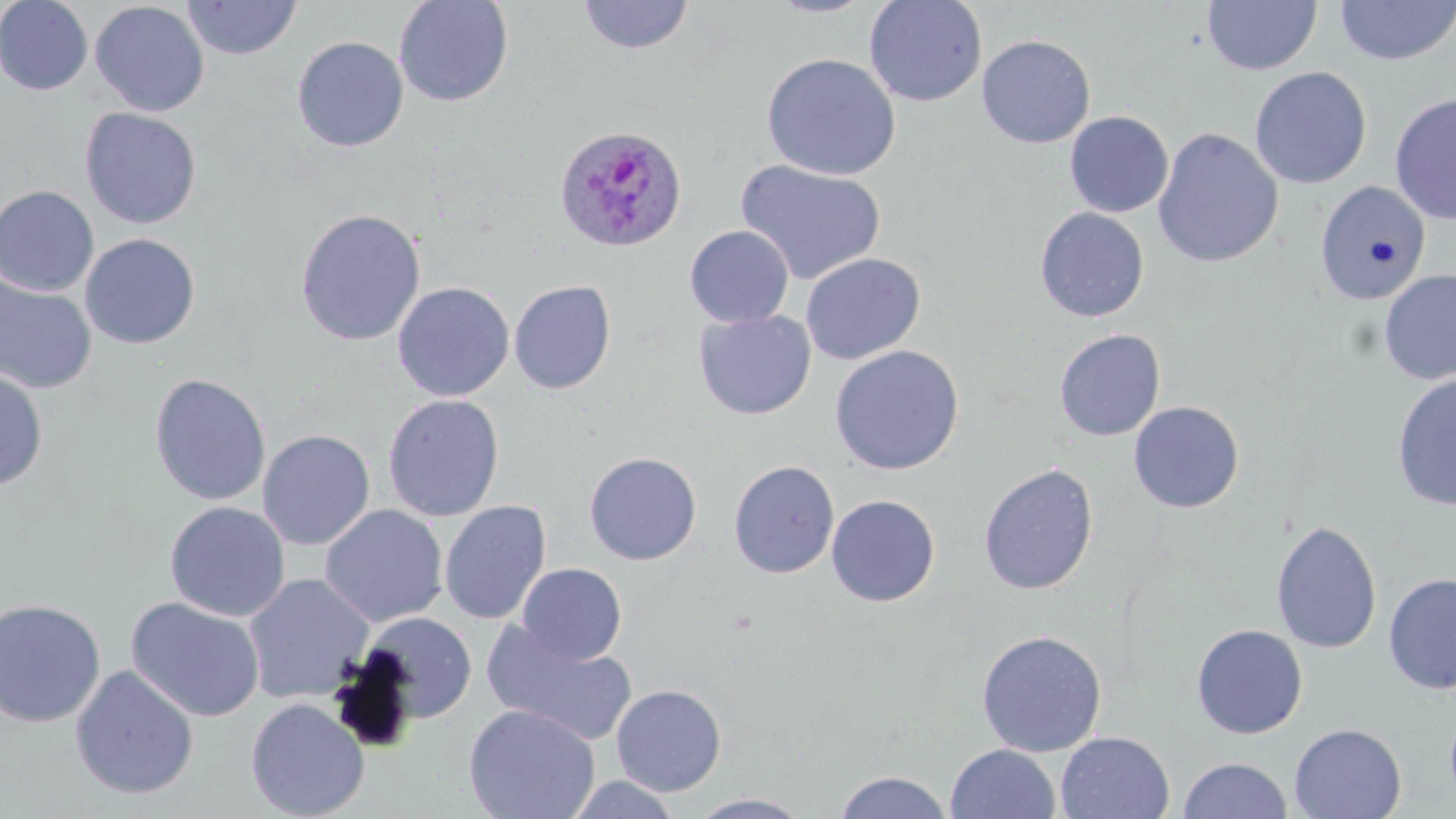 Approximate bounding boxes as named x1/y1/x2/y2 corners in pixels. Uninfected red blood cell locations: (x1=0, y1=0, x2=94, y2=95), (x1=182, y1=0, x2=302, y2=60), (x1=393, y1=0, x2=513, y2=107), (x1=577, y1=0, x2=695, y2=55), (x1=764, y1=0, x2=879, y2=18), (x1=864, y1=0, x2=987, y2=107), (x1=1202, y1=0, x2=1321, y2=75), (x1=1334, y1=0, x2=1456, y2=66), (x1=89, y1=1, x2=210, y2=117), (x1=976, y1=34, x2=1096, y2=148), (x1=292, y1=36, x2=409, y2=152), (x1=762, y1=53, x2=901, y2=180), (x1=1250, y1=66, x2=1372, y2=189), (x1=1389, y1=92, x2=1456, y2=225), (x1=79, y1=107, x2=202, y2=229), (x1=1065, y1=111, x2=1174, y2=217), (x1=1152, y1=127, x2=1284, y2=268), (x1=735, y1=159, x2=887, y2=285), (x1=1313, y1=181, x2=1431, y2=305), (x1=0, y1=185, x2=100, y2=297), (x1=1035, y1=207, x2=1150, y2=322), (x1=294, y1=209, x2=426, y2=346), (x1=685, y1=225, x2=794, y2=328), (x1=79, y1=233, x2=200, y2=349), (x1=799, y1=253, x2=926, y2=364), (x1=1378, y1=269, x2=1456, y2=385), (x1=0, y1=274, x2=97, y2=394), (x1=509, y1=279, x2=616, y2=395), (x1=392, y1=281, x2=515, y2=402), (x1=694, y1=310, x2=816, y2=420), (x1=1053, y1=329, x2=1165, y2=441), (x1=829, y1=345, x2=964, y2=476), (x1=0, y1=367, x2=49, y2=491), (x1=150, y1=373, x2=271, y2=506), (x1=1391, y1=374, x2=1456, y2=512), (x1=382, y1=394, x2=505, y2=522), (x1=1129, y1=401, x2=1244, y2=513), (x1=257, y1=429, x2=375, y2=550), (x1=584, y1=451, x2=702, y2=565), (x1=728, y1=460, x2=839, y2=579), (x1=978, y1=462, x2=1098, y2=595), (x1=826, y1=494, x2=940, y2=607), (x1=439, y1=500, x2=551, y2=625), (x1=164, y1=501, x2=290, y2=622), (x1=319, y1=504, x2=448, y2=627), (x1=1271, y1=520, x2=1382, y2=655), (x1=516, y1=563, x2=627, y2=665), (x1=1383, y1=572, x2=1456, y2=694), (x1=244, y1=573, x2=375, y2=704), (x1=126, y1=597, x2=265, y2=722), (x1=0, y1=599, x2=106, y2=728), (x1=361, y1=612, x2=477, y2=724), (x1=481, y1=621, x2=638, y2=747), (x1=1191, y1=623, x2=1308, y2=739), (x1=976, y1=629, x2=1107, y2=757), (x1=70, y1=664, x2=199, y2=800), (x1=610, y1=684, x2=727, y2=796), (x1=245, y1=697, x2=369, y2=819), (x1=1444, y1=700, x2=1456, y2=809), (x1=463, y1=704, x2=600, y2=819), (x1=1289, y1=723, x2=1407, y2=818), (x1=1055, y1=732, x2=1175, y2=819), (x1=945, y1=744, x2=1061, y2=819), (x1=1178, y1=757, x2=1293, y2=818), (x1=833, y1=770, x2=954, y2=818), (x1=565, y1=774, x2=683, y2=818), (x1=687, y1=793, x2=817, y2=818). Plasmodium ovale-infected red blood cell locations: (x1=554, y1=125, x2=687, y2=253). Slide-level diagnosis: Plasmodium ovale. Optical microscopy. Thin blood film. One field of a larger specimen. Image is 1456×819 pixels. May-Grünwald-Giemsa stain. 1000x magnification.